Outline each Plasmodium parasite.
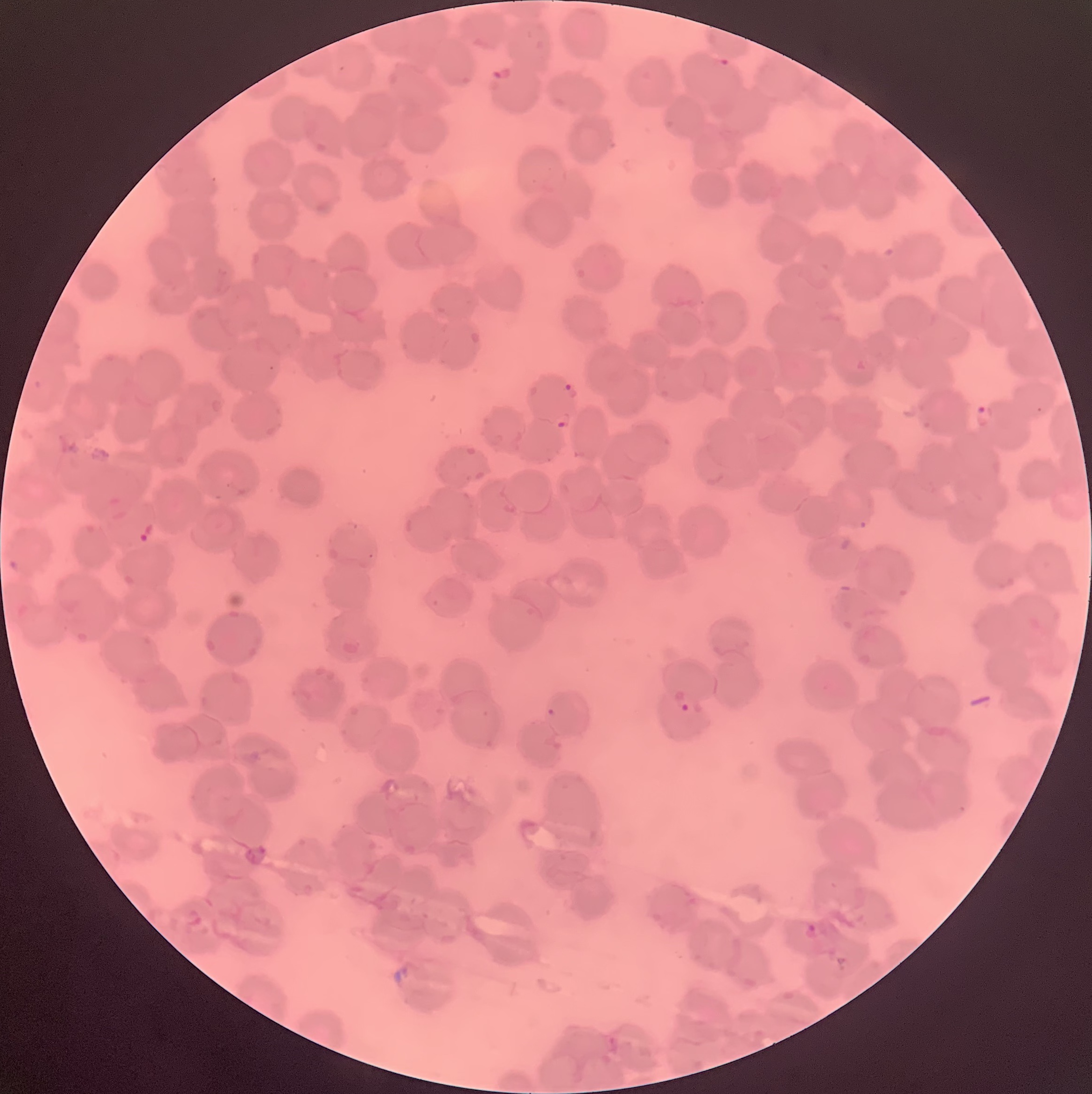

Approximate bounding boxes as (x1,y1)-(x2,y2) corner pairs in pixels.
Plasmodium parasites: (492,68)-(511,84), (560,383)-(579,400), (973,402)-(996,429), (554,411)-(571,429), (138,523)-(154,544), (672,689)-(690,713), (804,924)-(818,940).

Summary:
  - Preparation: thin blood film
  - Image size: 1092×1094 pixels
  - Modality: optical microscopy
  - Red blood cell morphology: rouleaux formation